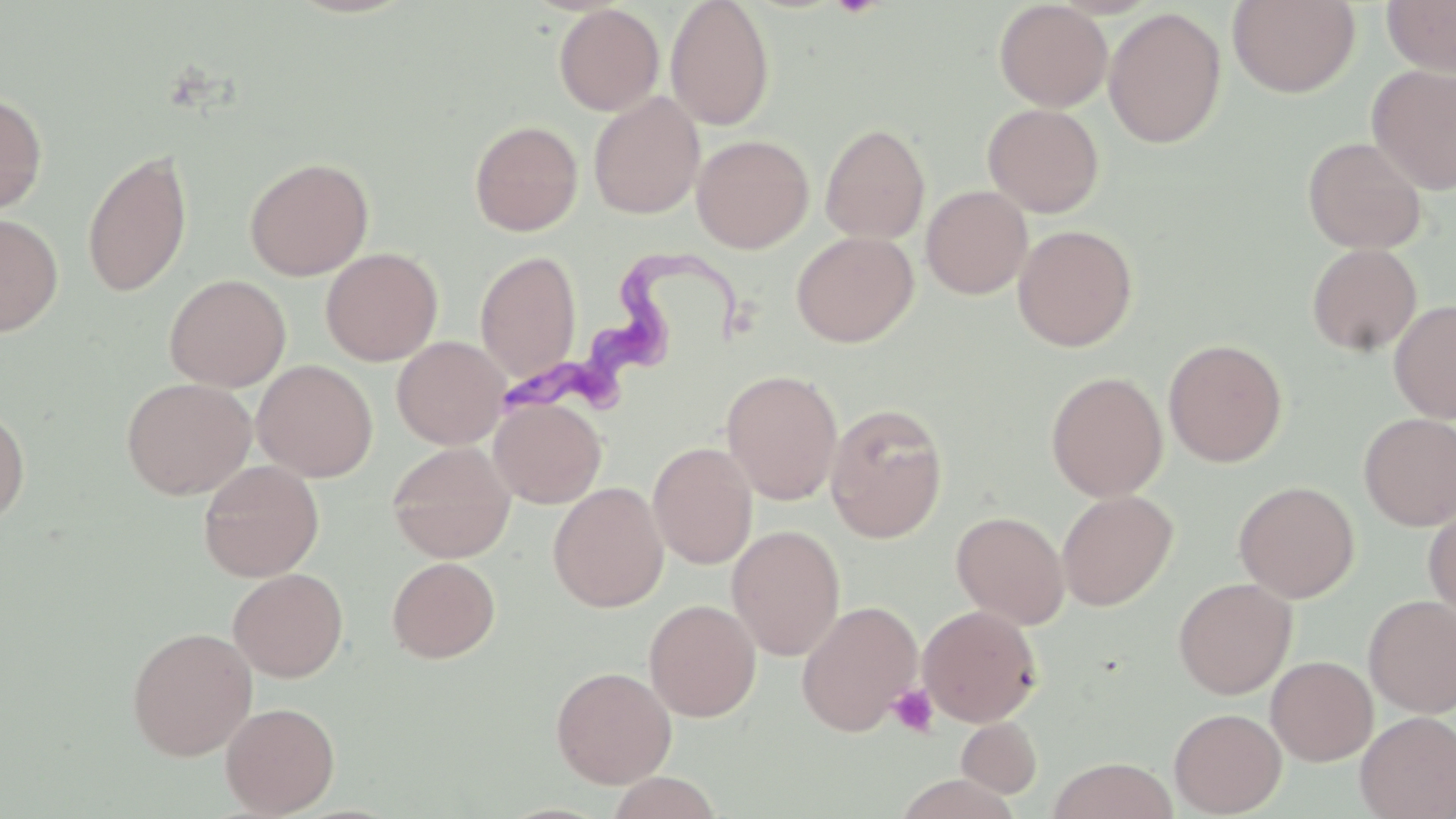
Approximate bounding boxes as [x1, y1, x2, y2] in pixels. Platelet locations: [888, 683, 939, 737]. Trypanosoma brucei locations: [495, 251, 741, 415]. Uninfected red blood cell locations: [665, 0, 775, 130], [1228, 0, 1360, 97], [1382, 0, 1456, 75], [993, 1, 1112, 111], [553, 4, 664, 116], [1103, 7, 1227, 149], [1367, 64, 1456, 194], [0, 91, 48, 216], [588, 91, 704, 219], [982, 103, 1104, 218], [469, 119, 583, 236], [820, 122, 930, 243], [692, 134, 813, 252], [1302, 136, 1427, 254], [82, 147, 194, 298], [244, 156, 374, 281], [921, 185, 1033, 299], [0, 211, 64, 337], [1012, 224, 1138, 351], [791, 231, 918, 347], [1306, 243, 1423, 357], [320, 247, 442, 366], [475, 250, 581, 382], [164, 274, 291, 391], [1389, 299, 1456, 423], [392, 336, 509, 449], [1164, 338, 1287, 467], [252, 359, 378, 481], [721, 369, 843, 505], [1046, 370, 1167, 502], [121, 377, 257, 499], [489, 397, 606, 508], [825, 402, 948, 543], [0, 403, 31, 528], [1358, 413, 1456, 530], [648, 441, 758, 569], [387, 442, 516, 562], [198, 460, 325, 581], [1233, 480, 1360, 602], [548, 482, 668, 612], [1057, 490, 1178, 610], [1424, 502, 1456, 623], [951, 510, 1070, 629], [727, 524, 846, 661], [386, 556, 501, 663], [228, 568, 348, 682], [1173, 577, 1297, 699], [1363, 595, 1456, 717], [643, 599, 762, 721], [796, 600, 923, 736], [918, 604, 1042, 727], [126, 626, 257, 760], [1266, 655, 1378, 765], [551, 665, 677, 788], [221, 702, 340, 817], [1169, 707, 1286, 817], [1356, 711, 1456, 819], [956, 717, 1042, 799], [1047, 757, 1179, 819], [603, 772, 723, 818]. Slide-level diagnosis: Trypanosoma brucei. Captured at 1000x magnification. Thin blood film. May-Grünwald-Giemsa stain. Single field of view. Light microscopy. Image is 1456×819 pixels.